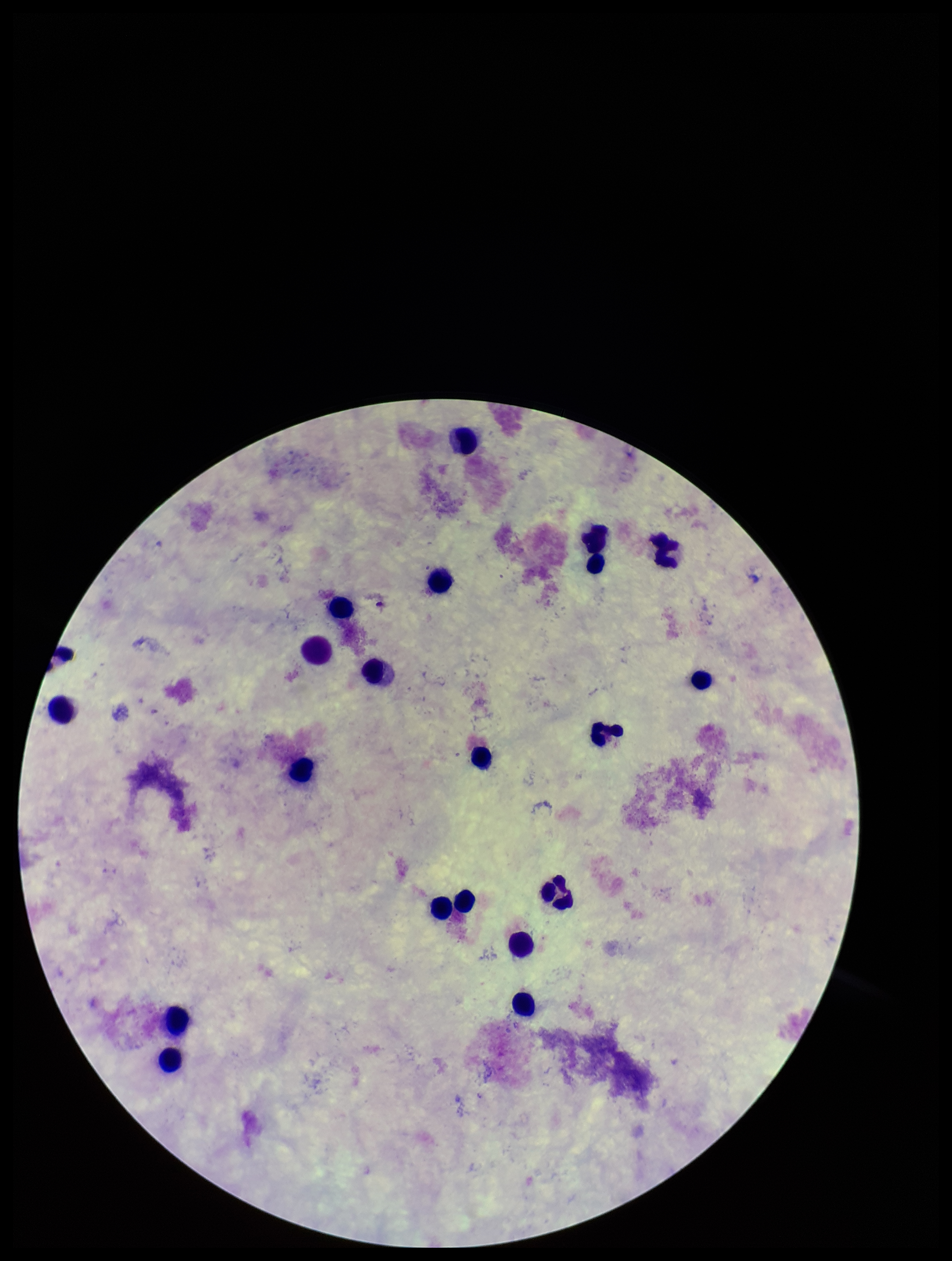
Summary:
  - Plasmodium parasites: none detected
  - Stain: Giemsa
  - Patient malaria status: negative
  - Parasite count: 0
  - Capture: smartphone photograph through the microscope eyepiece
  - Field of view: single
  - Image size: 952×1261 pixels
  - Leukocyte count: 20
  - Preparation: thick